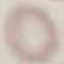

malaria status = uninfected
stain = Giemsa
capture = smartphone camera at the microscope eyepiece
image type = cell patch, automatically extracted from a larger field of view and resized to 64 × 64 pixels
preparation = thin blood smear